Classify this cell by malaria status.
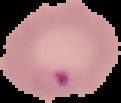
It is parasitized.

The area outside the segmented cell region is set to black. From a thin blood film. Image is 121×103 pixels.